Locate every blood parasite and identify its species.
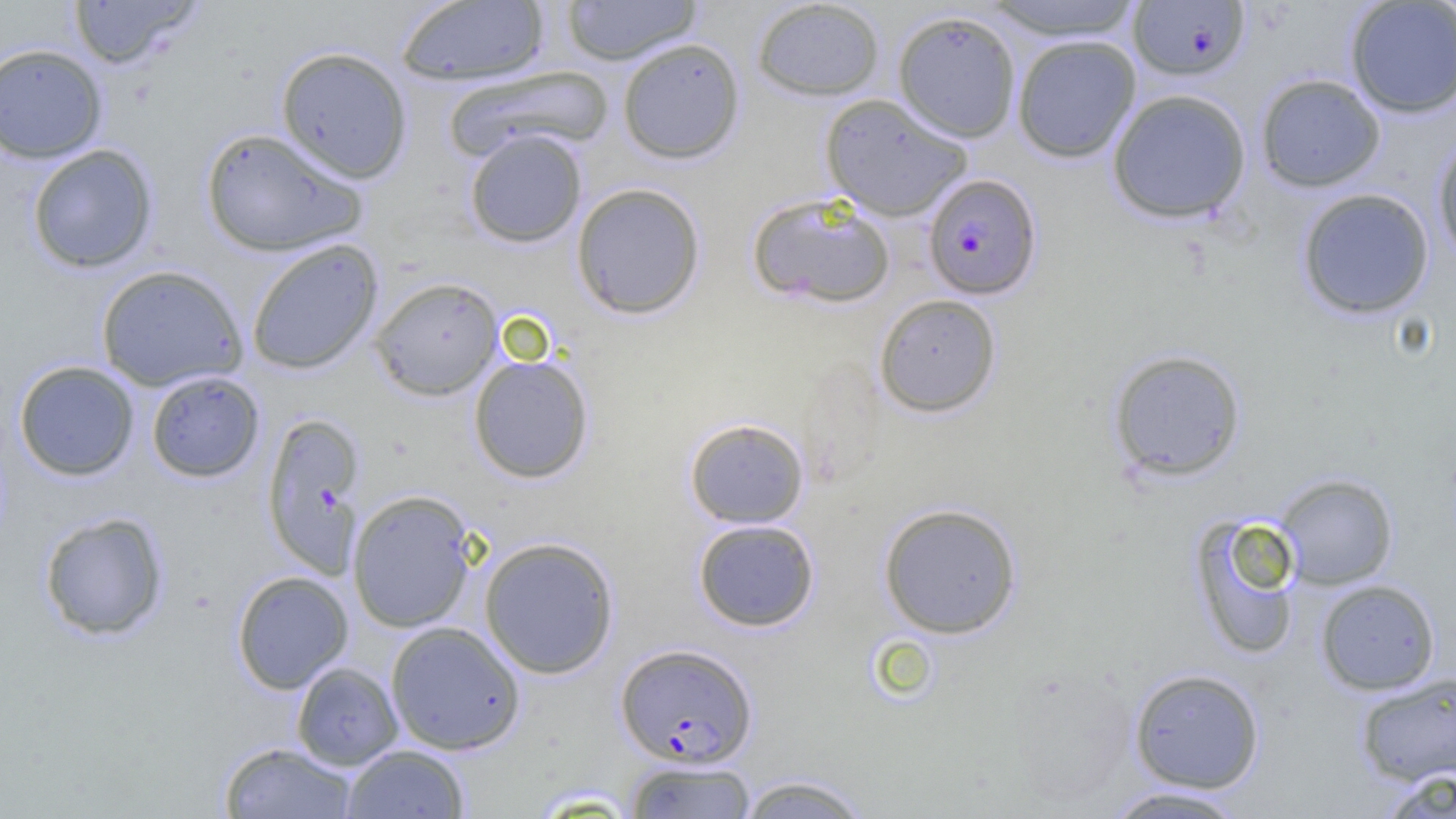
Approximate bounding boxes as (x1,y1)-(x2,y2) corner pairs in pixels.
Plasmodium falciparum-infected red blood cells: (1128,1)-(1250,81), (922,174)-(1042,300), (615,643)-(757,767).
No Plasmodium ovale, Plasmodium malariae, Plasmodium vivax, Babesia divergens, or Trypanosoma brucei observed.

Summary:
  - Uninfected red blood cell locations: (67,0)-(205,69), (395,0)-(551,86), (561,0)-(702,65), (751,0)-(885,101), (981,1)-(1146,40), (1345,1)-(1456,118), (892,10)-(1022,143), (1011,34)-(1141,164), (617,37)-(746,164), (0,43)-(108,164), (276,46)-(413,183), (441,65)-(612,163), (1255,73)-(1386,193), (1106,89)-(1251,224), (820,93)-(972,221), (200,127)-(368,257), (464,129)-(587,248), (1432,131)-(1456,268), (27,144)-(158,273), (571,183)-(706,320), (1296,187)-(1435,320), (747,192)-(897,309), (246,239)-(383,375), (95,265)-(248,392), (369,276)-(503,400), (874,293)-(1002,418), (1107,349)-(1246,482), (468,354)-(595,484), (13,360)-(140,481), (145,371)-(265,483), (261,411)-(366,576), (684,417)-(809,528), (1273,473)-(1398,590), (347,490)-(477,633), (878,503)-(1022,639), (38,511)-(170,641), (1188,512)-(1304,661), (693,518)-(820,632), (479,536)-(619,679), (231,570)-(353,693), (1315,579)-(1440,695), (385,621)-(526,755), (291,662)-(403,770), (1128,668)-(1265,794), (1355,671)-(1456,786), (218,741)-(358,818), (342,744)-(470,818), (623,760)-(758,818), (1378,768)-(1456,818), (735,774)-(873,818), (1101,786)-(1252,818)
  - Slide-level diagnosis: Plasmodium falciparum
  - Image size: 1456×819 pixels
  - Modality: optical microscopy
  - Field of view: one of a larger specimen
  - Preparation: thin blood smear
  - Magnification: 1000x